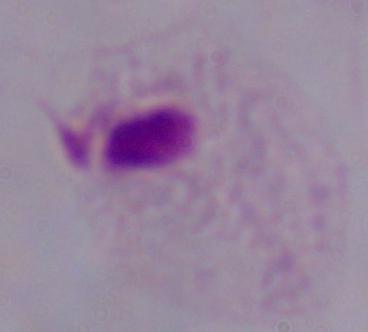
Summary:
  - Modality: photomicrograph
  - Magnification: 1000x
  - Identification: trichomonad